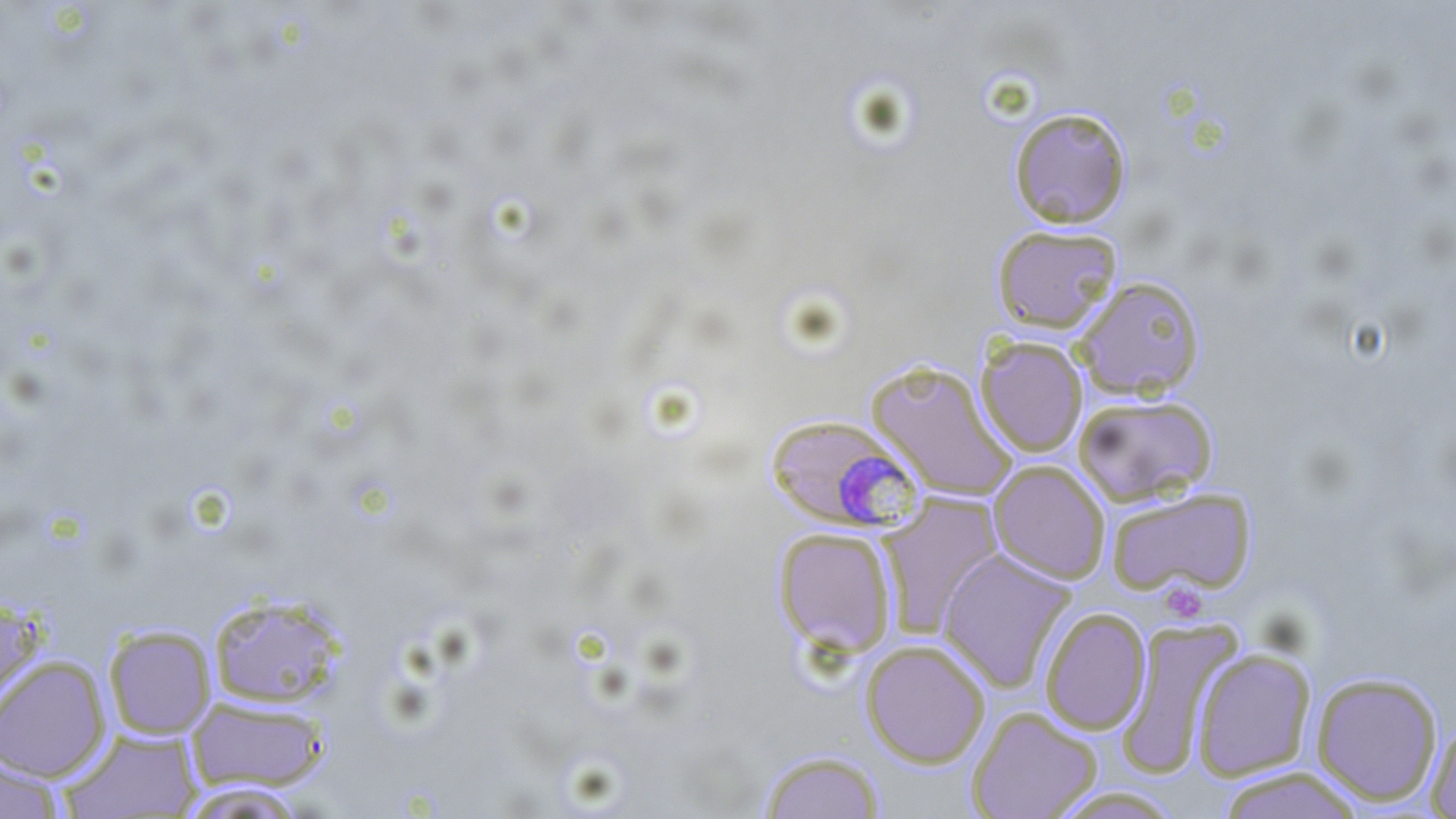
slide-level diagnosis = Plasmodium falciparum
magnification = 1000x
image size = 1456×819 pixels
field of view = single
platelet locations = approximate bounding boxes as (x1, y1, x2, y2) in pixels: (1158, 582, 1208, 622)
modality = optical microscopy
Plasmodium falciparum-infected red blood cell locations = approximate bounding boxes as (x1, y1, x2, y2) in pixels: (762, 413, 923, 533)
uninfected red blood cell locations = approximate bounding boxes as (x1, y1, x2, y2) in pixels: (1008, 106, 1133, 228), (991, 224, 1123, 333), (1073, 275, 1207, 400), (975, 336, 1088, 457), (866, 359, 1017, 500), (1073, 394, 1219, 507), (989, 460, 1110, 584), (1104, 487, 1256, 596), (878, 493, 1003, 637), (772, 526, 898, 656), (936, 548, 1077, 693), (207, 592, 348, 710), (0, 595, 46, 717), (1039, 606, 1152, 735), (1114, 620, 1244, 779), (103, 624, 217, 739), (860, 639, 991, 768), (1191, 648, 1316, 781), (0, 655, 111, 781), (1310, 671, 1444, 806), (185, 696, 331, 793), (967, 706, 1103, 819), (1425, 716, 1456, 818), (59, 728, 203, 818), (757, 749, 886, 819), (0, 753, 69, 819), (1215, 766, 1366, 819), (174, 781, 310, 818), (1045, 786, 1188, 818)
stain = May-Grünwald-Giemsa
preparation = thin blood smear